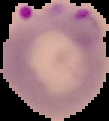
From a thin blood smear. Malaria status: parasitized. Cell region segmented out of the field of view; the surrounding area is masked to black. Image is 109×121 pixels.